Classify this cell by malaria status.
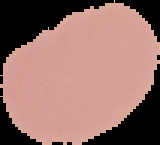

Uninfected.

image type = segmented cell region on a black background
preparation = thin blood film
image size = 160×145 pixels